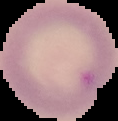
The area outside the segmented cell region is set to black. From a thin blood film. Malaria status: parasitized. Image is 118×121 pixels.